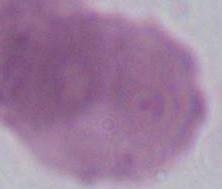
identification = red blood cell
modality = photomicrograph
magnification = 1000x